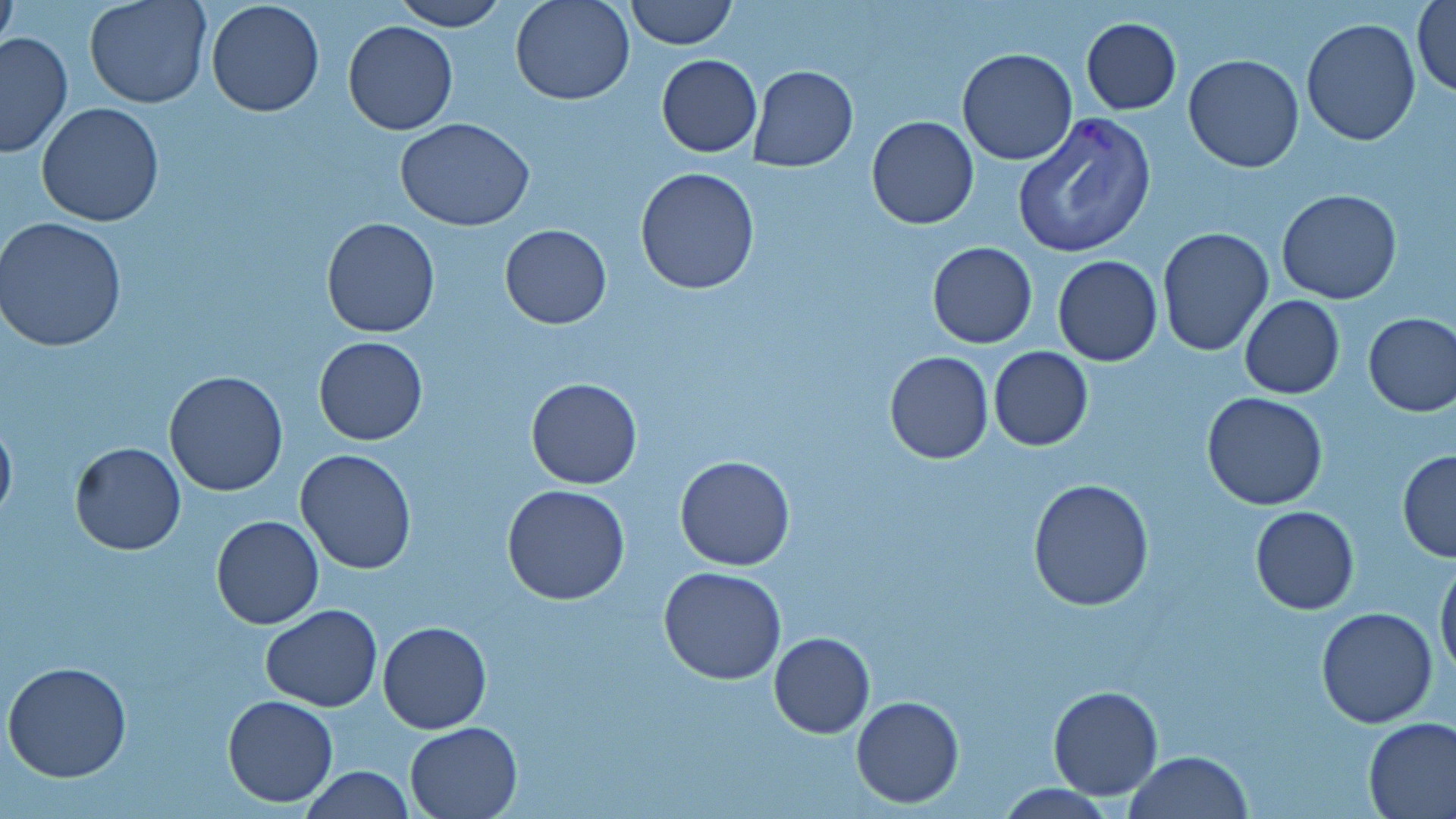

{
  "slide_level_diagnosis": "Plasmodium vivax",
  "image_size": "1456×819 pixels",
  "field_of_view": "one of a larger specimen",
  "modality": "light microscopy",
  "uninfected_red_blood_cell_locations": "approximate bounding boxes as [x1, y1, x2, y2] in pixels: [85, 0, 212, 109], [390, 0, 507, 31], [510, 0, 636, 106], [624, 0, 736, 50], [205, 1, 325, 117], [1410, 1, 1455, 98], [1, 3, 18, 57], [1081, 17, 1182, 114], [1300, 18, 1422, 146], [342, 21, 459, 136], [0, 31, 73, 159], [956, 47, 1078, 165], [656, 53, 762, 157], [1184, 55, 1305, 172], [748, 65, 858, 171], [37, 102, 164, 227], [866, 116, 979, 230], [394, 117, 536, 233], [635, 168, 760, 295], [1277, 189, 1403, 305], [320, 217, 441, 338], [1, 218, 128, 353], [498, 225, 613, 329], [1156, 227, 1273, 358], [927, 242, 1037, 348], [1052, 256, 1162, 367], [1239, 294, 1345, 400], [1363, 311, 1456, 417], [314, 336, 428, 446], [987, 346, 1093, 450], [884, 350, 994, 465], [163, 371, 288, 496], [526, 377, 643, 490], [1203, 392, 1328, 511], [0, 413, 17, 526], [69, 441, 186, 556], [296, 448, 417, 575], [1397, 450, 1456, 562], [674, 455, 797, 571], [1027, 479, 1155, 613], [502, 483, 632, 605], [1250, 506, 1360, 614], [211, 515, 324, 629], [1435, 556, 1456, 681], [658, 565, 786, 684], [260, 605, 382, 711], [1316, 607, 1438, 729], [376, 622, 491, 734], [769, 631, 875, 739], [2, 661, 132, 782], [1047, 684, 1163, 800], [222, 695, 339, 806], [850, 696, 964, 808], [1363, 716, 1456, 818], [404, 720, 523, 818], [1126, 751, 1253, 819], [298, 765, 416, 819], [994, 783, 1119, 817]",
  "magnification": "1000x",
  "preparation": "thin blood smear",
  "stain": "May-Grünwald-Giemsa",
  "plasmodium_vivax_infected_red_blood_cell_locations": "approximate bounding boxes as [x1, y1, x2, y2] in pixels: [1012, 112, 1156, 260]"
}